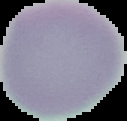

image size = 127×121 pixels
malaria status = uninfected
image type = segmented cell region on a black background
preparation = thin blood smear